Point out each Plasmodium parasite.
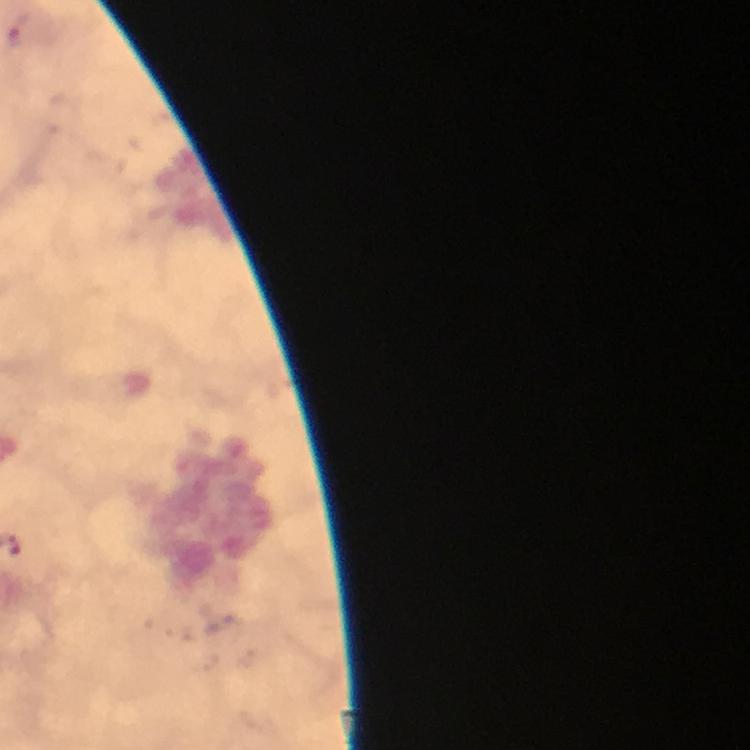
Approximate centers as (x, y) in pixels.
Plasmodium parasites: (26, 29).

Summary:
  - Capture: smartphone mounted on the microscope
  - Context: from a malaria diagnostic workup
  - Magnification: 100x
  - Immersion oil: applied
  - Image size: 750×750 pixels
  - Stain: Giemsa
  - Preparation: thick smear
  - Cropped from: a single field of view